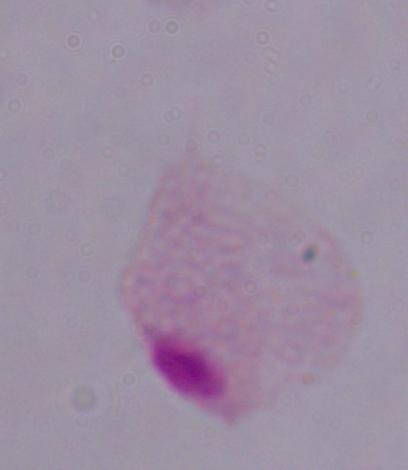
Summary:
  - Identification: trichomonad
  - Modality: photomicrograph
  - Magnification: 1000x